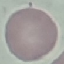
result = negative for malaria parasites
image type = cell patch, automatically extracted from a larger field of view and resized to 64 × 64 pixels
stain = Giemsa
capture = smartphone through the microscope eyepiece
preparation = thin smear